Classify this cell by malaria status.
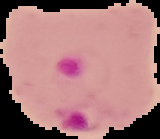
Parasitized.

Image is 160×139 pixels. The area outside the segmented cell region is set to black. From a thin blood smear.